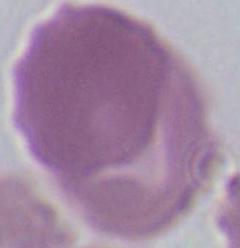
Captured at 1000x magnification. Micrograph. An erythrocyte is seen.